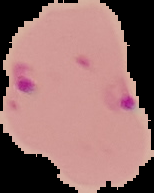
Result: Plasmodium parasites detected. The area outside the segmented cell region is set to black. Image is 154×193 pixels. From a thin blood film.